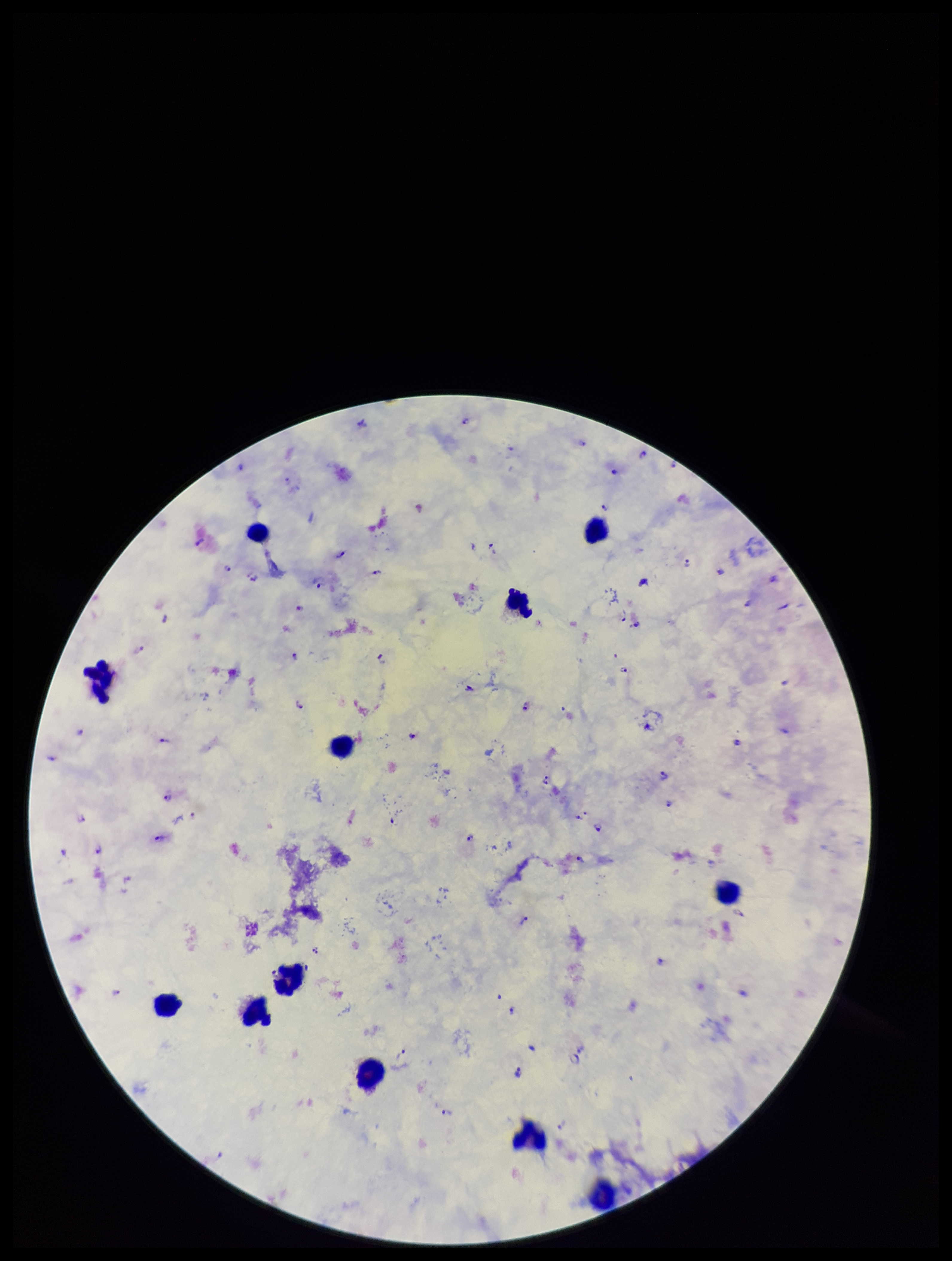

Summary:
  - Parasite count: 54
  - Species reported for this patient: Plasmodium falciparum
  - Stain: Giemsa
  - Plasmodium parasites: identified
  - Image size: 952×1261 pixels
  - Preparation: thick
  - Capture: smartphone photograph through the microscope eyepiece
  - Leukocyte count: 12
  - Field of view: single
  - Patient malaria status: positive